State which cell type is depicted.
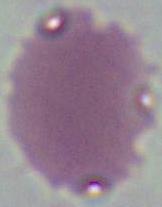

This is an erythrocyte.

Captured at 1000x magnification. Micrograph.